Give the extent of all Plasmodium vivax-infected red blood cells.
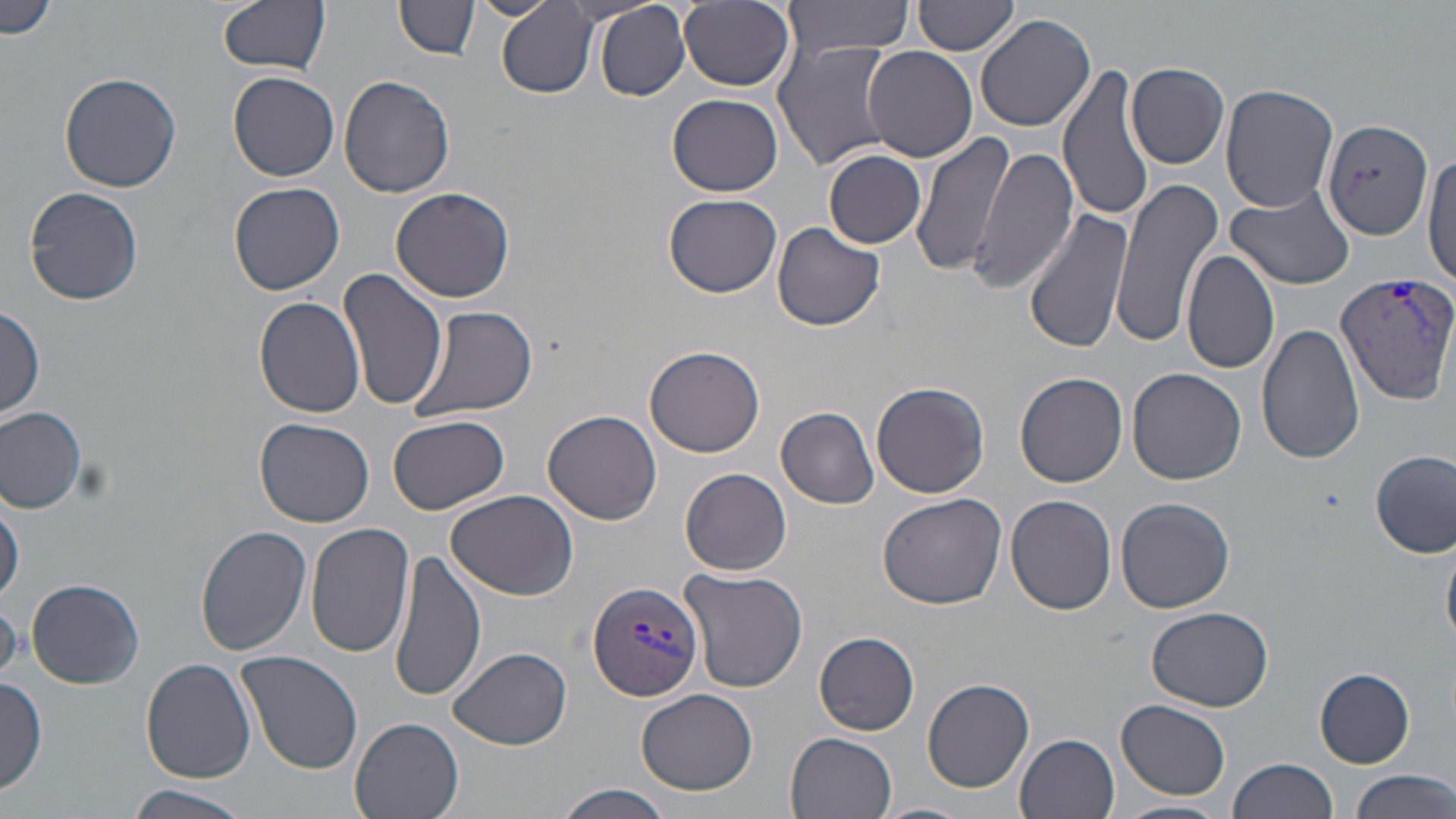
Approximate bounding boxes as (x1, y1, x2, y2) in pixels.
Plasmodium vivax-infected red blood cells: (1335, 270, 1455, 401), (586, 579, 706, 702).

Summary:
  - Uninfected red blood cell locations: (0, 0, 60, 41), (219, 0, 331, 75), (472, 0, 558, 19), (679, 0, 796, 91), (783, 0, 913, 55), (912, 0, 1020, 57), (395, 1, 479, 60), (496, 1, 601, 98), (595, 2, 689, 102), (974, 12, 1096, 134), (877, 37, 1071, 153), (773, 38, 899, 171), (864, 47, 978, 164), (1126, 63, 1229, 168), (1057, 64, 1153, 219), (230, 70, 340, 180), (60, 71, 182, 191), (339, 75, 455, 197), (1220, 83, 1339, 213), (668, 93, 782, 197), (1322, 117, 1433, 240), (910, 130, 1018, 276), (968, 145, 1079, 293), (1425, 147, 1456, 292), (824, 151, 929, 248), (1107, 173, 1225, 349), (229, 182, 345, 295), (24, 186, 143, 306), (390, 186, 514, 302), (1227, 186, 1354, 290), (398, 188, 523, 415), (664, 192, 782, 295), (1024, 209, 1134, 352), (773, 222, 884, 330), (1181, 248, 1279, 375), (339, 265, 447, 412), (255, 296, 366, 419), (1, 304, 45, 419), (408, 305, 538, 424), (1258, 320, 1367, 465), (645, 346, 765, 459), (1127, 367, 1246, 485), (1015, 372, 1128, 487), (873, 382, 990, 499), (0, 406, 86, 513), (777, 406, 879, 508), (543, 409, 662, 524), (386, 413, 511, 514), (256, 417, 374, 527), (1370, 449, 1454, 557), (681, 468, 791, 576), (446, 488, 579, 601), (1, 493, 23, 604), (877, 493, 1006, 609), (1004, 495, 1117, 615), (1114, 497, 1235, 612), (307, 523, 414, 658), (196, 524, 311, 656), (1442, 540, 1456, 650), (388, 549, 486, 703), (678, 566, 807, 692), (25, 578, 145, 689), (1146, 605, 1273, 712), (814, 632, 919, 735), (447, 647, 572, 749), (235, 650, 364, 773), (141, 658, 257, 783), (1314, 669, 1415, 768), (0, 675, 48, 797), (922, 678, 1034, 793), (636, 687, 759, 797), (1117, 699, 1232, 799), (349, 716, 464, 819), (784, 732, 897, 818), (1014, 732, 1119, 818), (1229, 757, 1340, 819), (1347, 768, 1453, 819), (129, 785, 252, 819), (553, 785, 676, 819), (1113, 799, 1230, 819), (869, 801, 975, 819)
  - Slide-level diagnosis: Plasmodium vivax
  - Magnification: 1000x
  - Preparation: thin blood film
  - Stain: May-Grünwald-Giemsa
  - Modality: light microscopy
  - Image size: 1456×819 pixels
  - Field of view: single